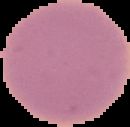

image type = segmented cell region with the area outside set to black
preparation = thin blood film
image size = 130×127 pixels
malaria status = uninfected